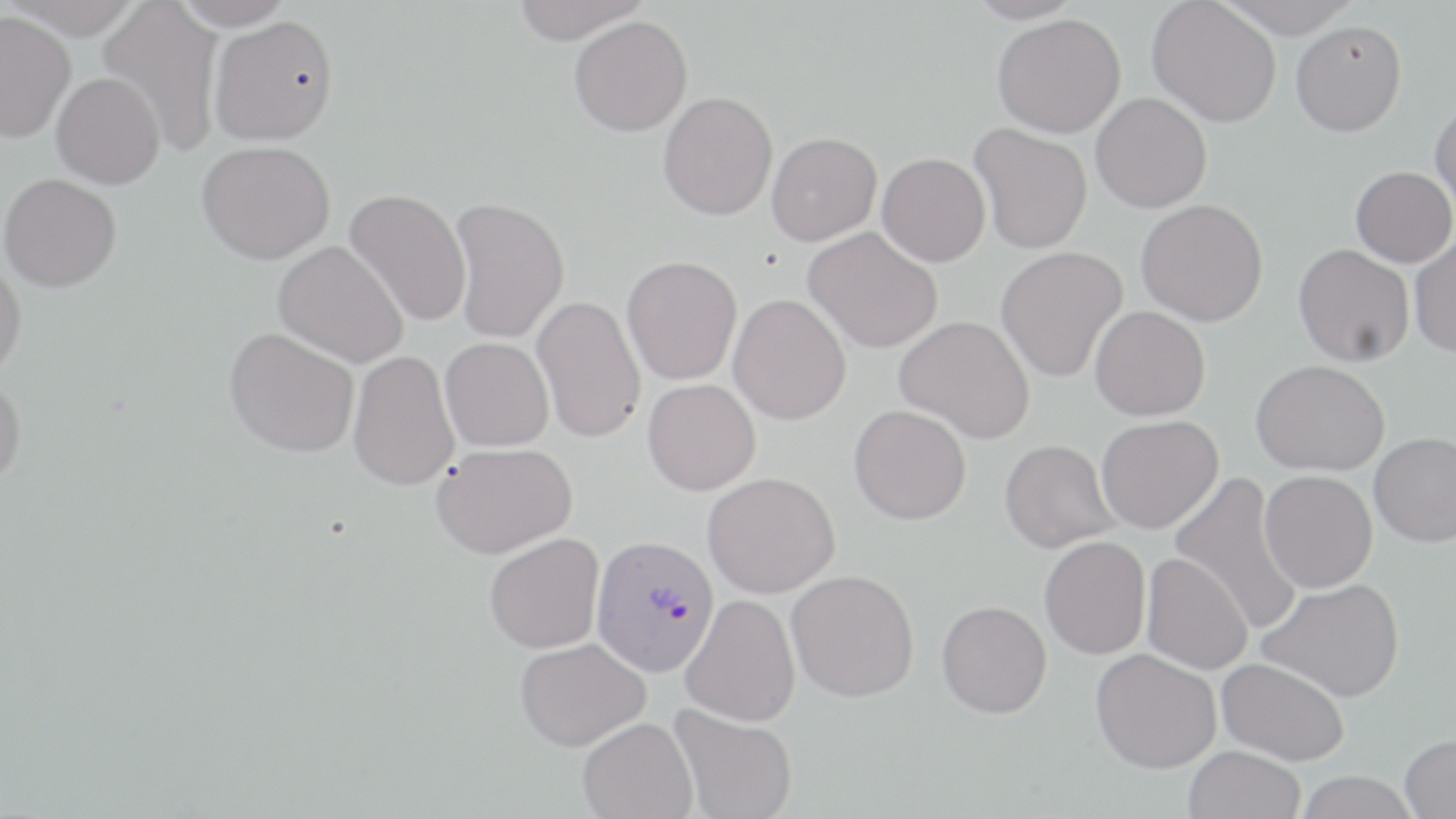

Summary:
  - Coordinate format: approximate bounding boxes as named x1/y1/x2/y2 corners in pixels
  - Uninfected red blood cell locations: (x1=3, y1=0, x2=145, y2=39), (x1=172, y1=0, x2=297, y2=30), (x1=510, y1=0, x2=652, y2=43), (x1=964, y1=0, x2=1084, y2=25), (x1=1214, y1=0, x2=1362, y2=39), (x1=1147, y1=1, x2=1281, y2=127), (x1=98, y1=2, x2=225, y2=156), (x1=0, y1=11, x2=76, y2=142), (x1=992, y1=13, x2=1126, y2=137), (x1=208, y1=16, x2=338, y2=145), (x1=569, y1=16, x2=692, y2=137), (x1=1290, y1=20, x2=1406, y2=136), (x1=51, y1=72, x2=165, y2=189), (x1=658, y1=91, x2=777, y2=220), (x1=1091, y1=93, x2=1212, y2=213), (x1=1430, y1=99, x2=1456, y2=219), (x1=969, y1=123, x2=1093, y2=253), (x1=766, y1=132, x2=882, y2=245), (x1=197, y1=141, x2=335, y2=264), (x1=877, y1=153, x2=990, y2=266), (x1=1351, y1=166, x2=1455, y2=267), (x1=0, y1=173, x2=122, y2=293), (x1=344, y1=189, x2=471, y2=327), (x1=448, y1=196, x2=570, y2=343), (x1=1136, y1=199, x2=1268, y2=326), (x1=803, y1=227, x2=942, y2=354), (x1=1410, y1=236, x2=1456, y2=357), (x1=273, y1=240, x2=409, y2=368), (x1=1293, y1=244, x2=1415, y2=367), (x1=996, y1=247, x2=1128, y2=383), (x1=621, y1=255, x2=743, y2=385), (x1=0, y1=258, x2=27, y2=380), (x1=728, y1=293, x2=851, y2=425), (x1=531, y1=295, x2=646, y2=443), (x1=1090, y1=306, x2=1210, y2=421), (x1=894, y1=315, x2=1036, y2=444), (x1=224, y1=327, x2=359, y2=458), (x1=440, y1=337, x2=554, y2=451), (x1=347, y1=350, x2=460, y2=491), (x1=1251, y1=360, x2=1389, y2=476), (x1=0, y1=375, x2=26, y2=490), (x1=643, y1=379, x2=761, y2=495), (x1=849, y1=404, x2=971, y2=525), (x1=1096, y1=415, x2=1224, y2=533), (x1=1369, y1=431, x2=1456, y2=546), (x1=999, y1=439, x2=1120, y2=552), (x1=431, y1=442, x2=577, y2=558), (x1=1259, y1=470, x2=1378, y2=593), (x1=702, y1=471, x2=840, y2=598), (x1=1169, y1=472, x2=1304, y2=636), (x1=484, y1=533, x2=604, y2=653), (x1=1039, y1=536, x2=1151, y2=659), (x1=1141, y1=552, x2=1253, y2=675), (x1=786, y1=569, x2=919, y2=702), (x1=1258, y1=578, x2=1405, y2=702), (x1=680, y1=593, x2=801, y2=726), (x1=936, y1=600, x2=1052, y2=718), (x1=515, y1=637, x2=650, y2=751), (x1=1091, y1=648, x2=1221, y2=773), (x1=1217, y1=657, x2=1349, y2=765), (x1=669, y1=704, x2=797, y2=819), (x1=577, y1=717, x2=698, y2=819), (x1=1399, y1=735, x2=1456, y2=818), (x1=1183, y1=745, x2=1305, y2=819), (x1=1295, y1=771, x2=1419, y2=819)
  - Plasmodium vivax-infected red blood cell locations: (x1=591, y1=534, x2=720, y2=676)
  - Slide-level diagnosis: Plasmodium vivax
  - Modality: light microscopy
  - Field of view: single
  - Stain: May-Grünwald-Giemsa
  - Preparation: thin blood film
  - Image size: 1456×819 pixels
  - Magnification: 1000x